Assess this cell for malaria.
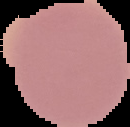

It is uninfected.

preparation = thin blood film
image size = 130×127 pixels
image type = segmented cell region on a black background